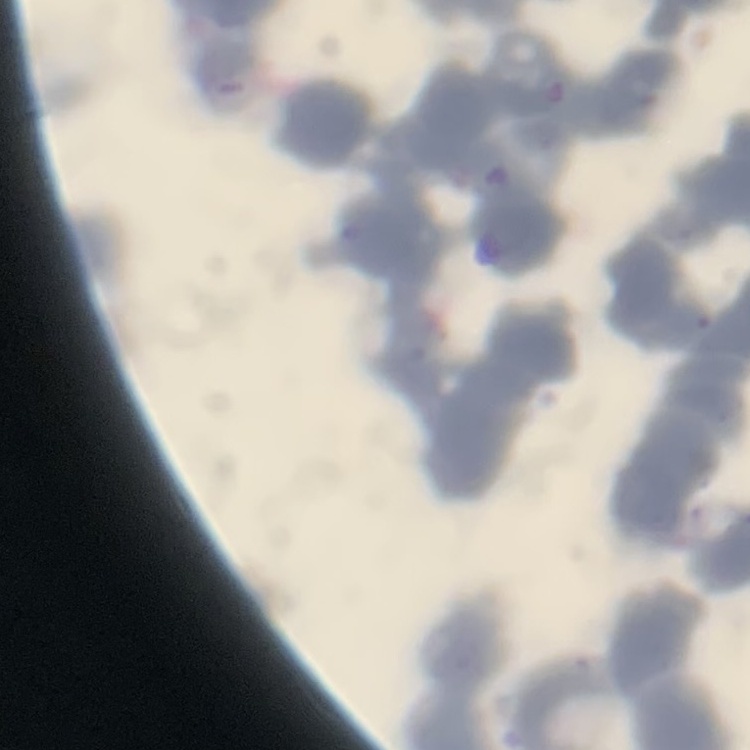

The red blood cells exhibit rouleaux formation. One tile cut from a larger photomicrograph. Stained with either Field's or Giemsa. Thin peripheral smear.